State the blood parasite species.
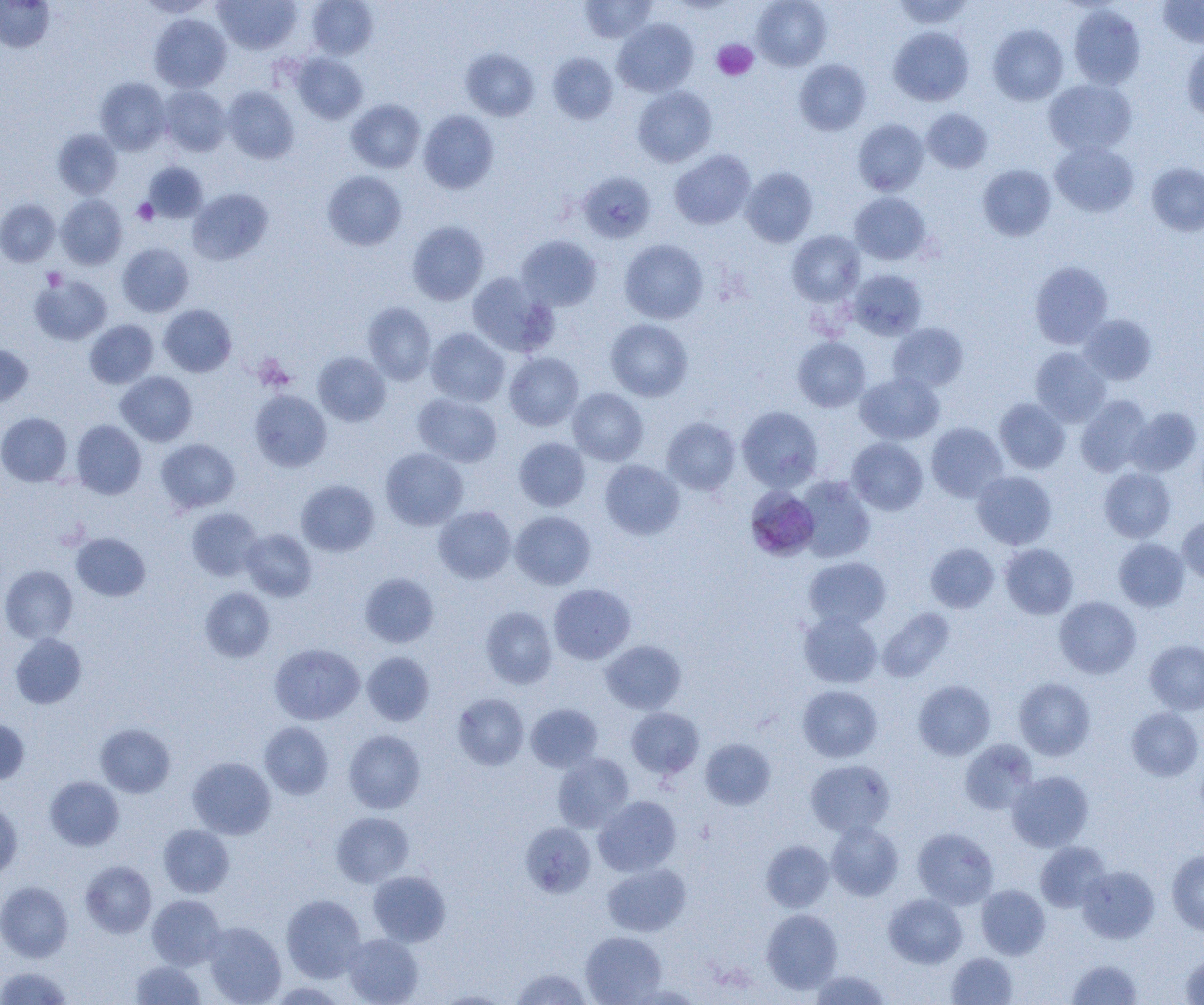
Plasmodium malariae.

Summary:
  - Coordinate format: approximate bounding boxes as [x1, y1, x2, y2] in pixels
  - Plasmodium malariae-infected red blood cell locations: [744, 486, 820, 561]
  - Uninfected red blood cell locations: [138, 0, 216, 18], [213, 0, 301, 54], [307, 0, 378, 60], [752, 0, 832, 70], [891, 0, 974, 29], [1157, 0, 1204, 47], [0, 1, 54, 52], [579, 1, 657, 43], [1068, 4, 1146, 89], [149, 13, 231, 92], [613, 19, 698, 97], [988, 24, 1068, 105], [889, 26, 974, 105], [1182, 40, 1204, 122], [461, 48, 539, 121], [548, 52, 618, 124], [292, 53, 367, 124], [794, 59, 871, 135], [95, 78, 171, 155], [1043, 78, 1136, 155], [158, 86, 232, 156], [632, 86, 717, 167], [223, 87, 299, 164], [346, 99, 425, 173], [921, 108, 992, 173], [418, 110, 499, 194], [853, 119, 929, 196], [53, 129, 122, 198], [1050, 141, 1139, 217], [670, 150, 756, 229], [143, 162, 207, 223], [1146, 162, 1204, 236], [978, 164, 1057, 241], [741, 167, 818, 247], [322, 171, 406, 251], [577, 171, 657, 243], [188, 188, 273, 265], [849, 192, 931, 265], [56, 195, 127, 269], [0, 199, 60, 267], [407, 221, 488, 305], [787, 230, 865, 305], [516, 235, 602, 311], [619, 239, 708, 323], [116, 242, 193, 317], [1030, 261, 1114, 349], [848, 269, 927, 340], [466, 271, 557, 357], [30, 274, 111, 346], [363, 302, 436, 384], [159, 305, 236, 377], [1079, 314, 1157, 385], [605, 318, 693, 401], [85, 319, 159, 388], [888, 323, 968, 393], [426, 328, 509, 406], [793, 337, 871, 411], [0, 344, 33, 407], [1030, 347, 1111, 426], [313, 352, 390, 426], [504, 352, 583, 430], [116, 371, 197, 446], [855, 373, 944, 445], [568, 388, 648, 465], [250, 390, 332, 471], [413, 393, 502, 467], [1076, 395, 1153, 477], [995, 398, 1070, 473], [737, 406, 823, 492], [1126, 407, 1201, 477], [0, 412, 72, 487], [662, 417, 741, 495], [71, 420, 146, 498], [925, 422, 1008, 502], [514, 437, 590, 511], [156, 438, 239, 514], [847, 438, 928, 515], [380, 448, 468, 530], [600, 459, 684, 540], [1099, 467, 1176, 542], [972, 470, 1056, 549], [795, 476, 875, 563], [296, 480, 379, 556], [433, 506, 516, 583], [186, 507, 263, 581], [510, 511, 595, 589], [1177, 516, 1204, 584], [240, 529, 317, 601], [71, 533, 150, 601], [1114, 538, 1189, 611], [926, 543, 999, 612], [1000, 543, 1078, 619], [804, 556, 891, 629], [0, 565, 78, 644], [360, 573, 438, 647], [549, 584, 636, 664], [200, 587, 275, 663], [1055, 596, 1141, 678], [480, 606, 557, 689], [878, 608, 955, 682], [799, 611, 883, 688], [10, 634, 86, 708], [1145, 639, 1204, 715], [601, 640, 686, 714], [269, 643, 364, 724], [362, 651, 434, 725], [1014, 678, 1095, 760], [913, 680, 996, 760], [798, 685, 882, 762], [453, 693, 529, 770], [526, 703, 602, 772], [1126, 707, 1203, 781], [626, 708, 704, 779], [0, 718, 30, 784], [259, 722, 334, 799], [95, 724, 175, 797], [344, 730, 425, 813], [700, 738, 775, 809], [959, 739, 1038, 815], [552, 753, 634, 832], [187, 757, 276, 839], [805, 759, 896, 837], [1007, 770, 1093, 851], [45, 776, 124, 850], [593, 796, 681, 876], [0, 800, 22, 879], [331, 812, 414, 887], [520, 822, 596, 897], [826, 822, 903, 900], [158, 824, 234, 897], [912, 828, 999, 908], [761, 840, 833, 912], [1035, 841, 1111, 912], [1166, 850, 1204, 936], [80, 860, 156, 938], [602, 863, 691, 936], [1077, 865, 1159, 943], [368, 871, 450, 947], [0, 881, 73, 962], [976, 884, 1050, 959], [883, 893, 967, 968], [281, 894, 366, 982], [147, 895, 226, 969], [761, 908, 842, 994], [202, 922, 286, 1005], [581, 931, 666, 1004], [343, 934, 423, 1005], [946, 952, 1018, 1004], [1180, 953, 1204, 1004], [1067, 959, 1142, 1005], [130, 960, 206, 1004], [0, 967, 72, 1005], [510, 968, 594, 1004], [812, 970, 890, 1005], [432, 990, 515, 1004]
  - Platelet locations: [712, 39, 758, 81], [133, 199, 158, 226], [43, 268, 66, 290]
  - Modality: light microscopy
  - Preparation: thin blood film
  - Magnification: 1000x
  - Field of view: single
  - Image size: 1204×1005 pixels